Classify this cell by malaria status.
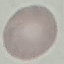

It is uninfected.

Summary:
  - Preparation: thin smear
  - Image type: cell patch, automatically extracted from a larger field of view and resized to 64 × 64 pixels
  - Capture: smartphone camera at the microscope eyepiece
  - Stain: Giemsa